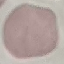
Malaria status: uninfected. Giemsa stain. Photographed with a smartphone camera at the microscope eyepiece. Thin blood film. Cell patch, automatically extracted from a larger field of view and resized to 64 × 64 pixels.